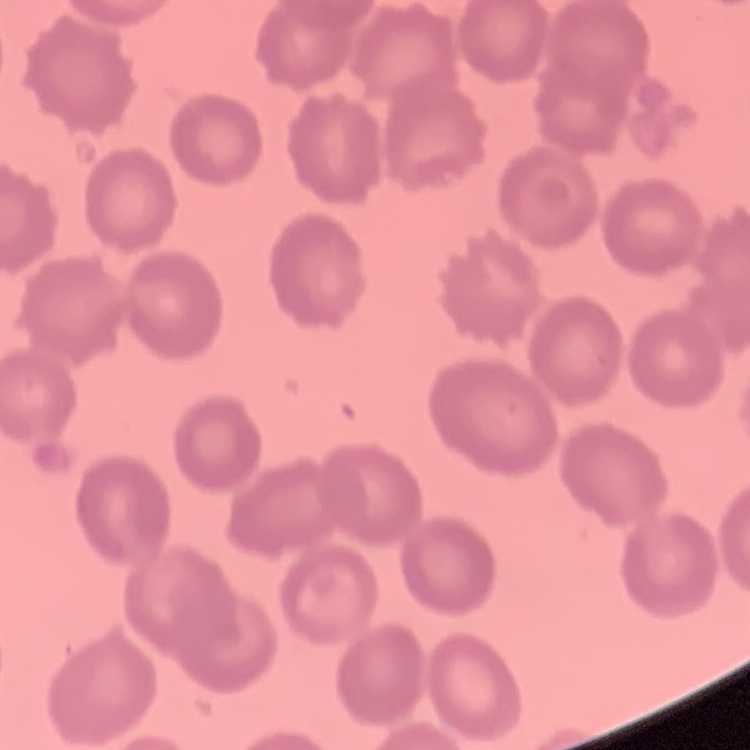

The red blood cells show no rouleaux formation. Field's or Giemsa stain. Thin blood smear. Square crop of a larger photomicrograph.